Classify this cell by malaria status.
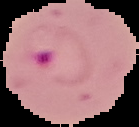

Parasitized.

From a thin blood smear. Image is 139×127 pixels. Cell region segmented out of the field of view; the surrounding area is masked to black.